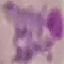 Result: malaria parasites identified. Acquired by smartphone through the microscope eyepiece. Thin blood film. Giemsa stain. Automatically extracted cell patch, resized to 64 × 64 pixels.